Give the position of each Plasmodium falciparum parasite with its life-cycle stage, each leukocyte, and any debris.
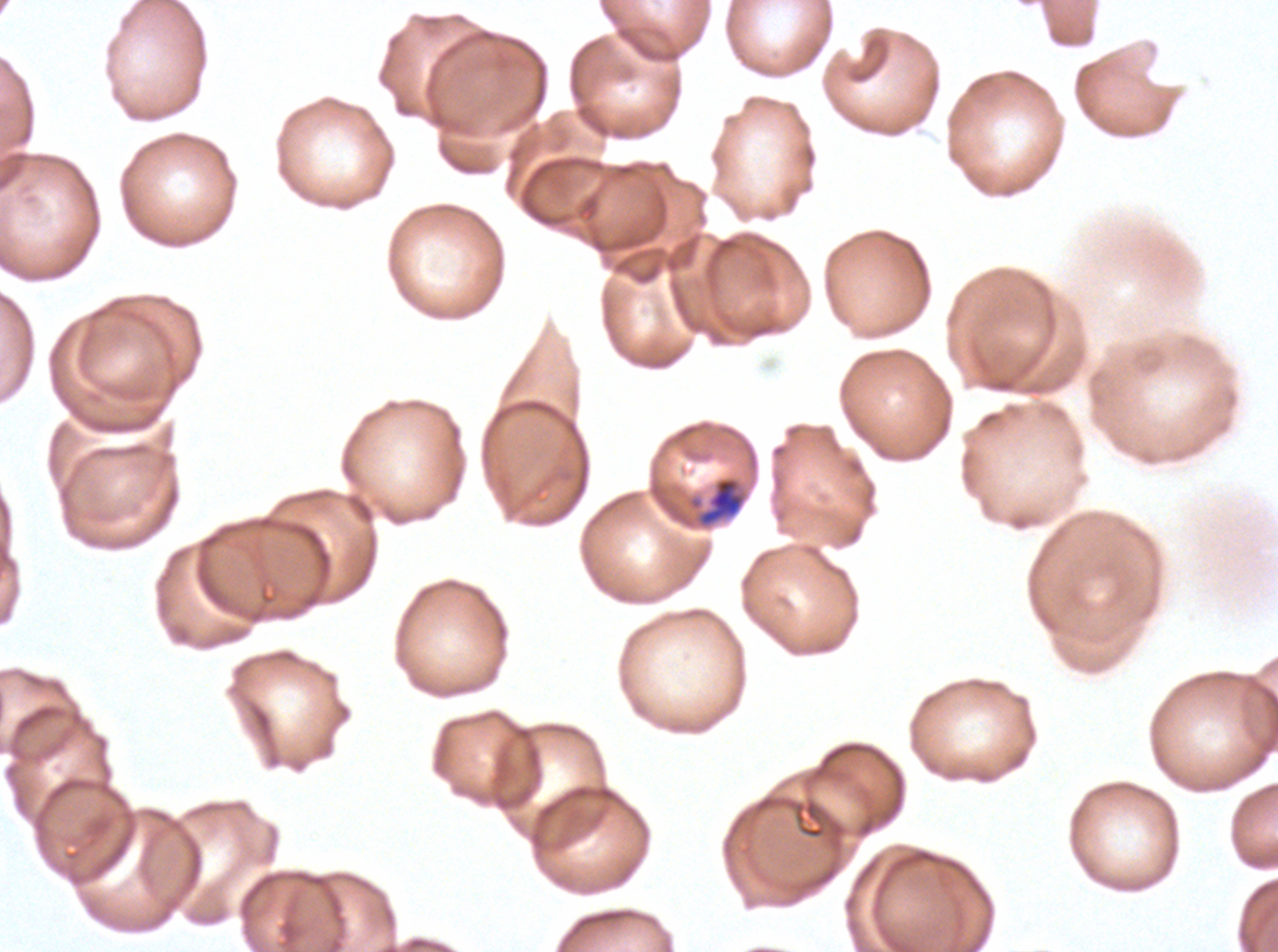

Approximate bounding rectangles given as corner coordinates in pixels from the top-left.
Mid trophozoites: (x1=699, y1=477, x2=744, y2=526).
Debris: (x1=793, y1=798, x2=827, y2=839).
No rings, late-ring/early-trophozoite forms, late trophozoites, early schizonts, late schizonts, segmenters, gametocytes, or leukocytes observed.

Giemsa-stained preparation. Plasmodium falciparum from a patient in The Gambia, cultured ex vivo for 24 to 48 hours. Thin blood smear. Image is 1278×952 pixels. One sub-image of a larger composite.